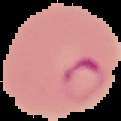
Result: Plasmodium parasites detected. From a thin blood smear. Image is 121×121 pixels. Segmented cell region on a black background.